State which cell type is depicted.
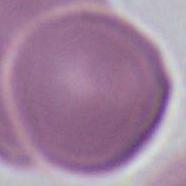
This is an erythrocyte.

magnification: 1000x
modality: micrograph